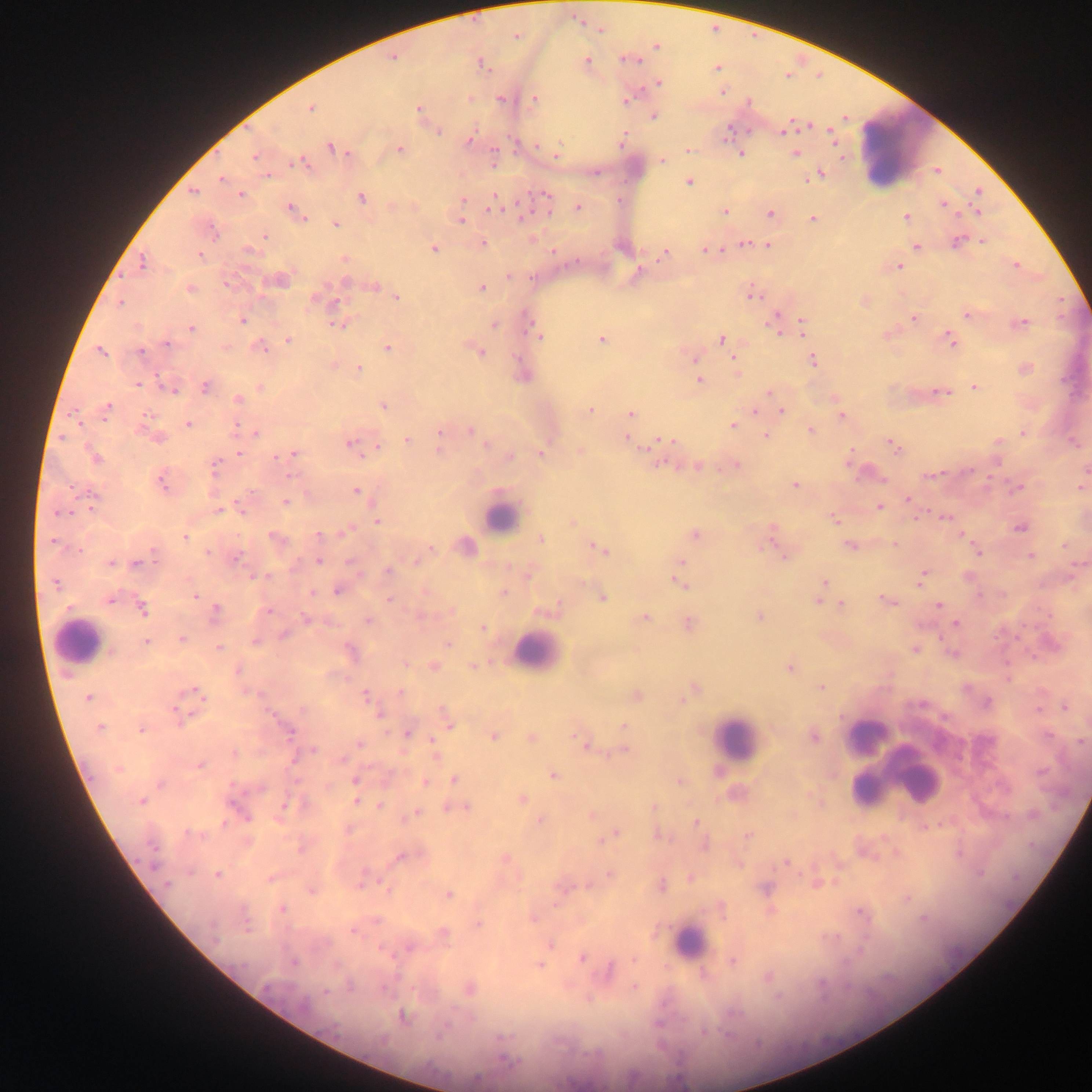
Approximate centers as (x, y) in pixels.
Summary:
  - Malaria parasite locations: (600, 30), (517, 36), (656, 47), (393, 58), (631, 60), (586, 61), (482, 65), (717, 67), (658, 83), (722, 91), (503, 100), (535, 100), (627, 101), (419, 108), (311, 109), (653, 116), (785, 129), (438, 130), (729, 130), (831, 132), (470, 138), (622, 141), (332, 148), (399, 149), (689, 149), (741, 154), (795, 154), (556, 155), (253, 157), (661, 160), (297, 163), (820, 174), (221, 179), (689, 182), (979, 190), (193, 192), (241, 195), (545, 195), (361, 198), (463, 199), (495, 204), (944, 204), (578, 206), (291, 208), (725, 211), (976, 211), (296, 212), (769, 213), (906, 217), (813, 218), (461, 221), (336, 224), (265, 237), (982, 241), (957, 242), (483, 244), (745, 244), (768, 245), (917, 246), (434, 248), (250, 251), (708, 251), (665, 254), (199, 255), (345, 259), (142, 263), (1015, 266), (899, 267), (280, 280), (346, 282), (227, 284), (374, 286), (482, 288), (191, 289), (753, 295), (396, 296), (316, 299), (120, 302), (967, 315), (775, 318), (913, 319), (242, 321), (1021, 322), (803, 324), (340, 325), (495, 325), (533, 326), (191, 328), (537, 334), (288, 340), (601, 340), (722, 340), (950, 340), (167, 343), (260, 346), (387, 347), (101, 351), (141, 353), (480, 353), (695, 359), (813, 360), (358, 369), (1025, 369), (700, 381), (139, 383), (205, 387), (975, 387), (169, 388), (260, 389), (941, 391), (770, 393), (238, 399), (383, 406), (108, 407), (590, 410), (755, 411), (782, 411), (631, 415), (841, 416), (189, 424), (732, 424), (236, 427), (470, 431), (811, 431), (440, 432), (256, 433), (1023, 433), (155, 436), (766, 436), (407, 439), (628, 439), (668, 440), (1075, 443), (349, 444), (487, 444), (894, 445), (378, 447), (440, 450), (580, 451), (541, 452), (239, 453), (293, 454), (285, 456), (96, 457), (510, 457), (736, 465), (214, 466), (698, 467), (1086, 469), (970, 471), (931, 476), (161, 483), (795, 485), (1017, 488), (1081, 488), (356, 491), (93, 497), (908, 499), (285, 502), (879, 507), (217, 510), (243, 511), (61, 513), (945, 517), (834, 520), (377, 521), (572, 522), (1020, 527), (345, 532), (318, 534), (694, 534), (185, 537), (275, 537), (540, 539), (771, 540), (53, 542), (466, 545), (850, 546), (430, 547), (776, 548), (601, 549), (208, 553), (979, 553), (783, 555), (1030, 555), (238, 557), (319, 561), (417, 561), (111, 563), (681, 563), (136, 564), (388, 572), (265, 575), (258, 577), (921, 579), (823, 582), (680, 583), (56, 584), (338, 591), (503, 592), (312, 593), (194, 595), (602, 597), (111, 600), (388, 600), (887, 601), (818, 602), (842, 605), (938, 606), (143, 609), (267, 611), (215, 612), (760, 616), (644, 618), (306, 619), (368, 621), (688, 623), (956, 623), (482, 627), (284, 635), (182, 639), (146, 642), (255, 642), (447, 643), (219, 648), (915, 650), (351, 653), (953, 653), (434, 666), (473, 666), (789, 669), (238, 671), (821, 688), (694, 689), (196, 691), (400, 692), (365, 695), (637, 696), (88, 697), (683, 700), (987, 702), (923, 704), (1064, 707), (303, 709), (1039, 709), (443, 711), (177, 712), (379, 716), (449, 725), (623, 725), (100, 727), (141, 729), (289, 731), (407, 734), (1048, 735), (493, 737), (814, 737), (531, 738), (1082, 742), (583, 743), (360, 744), (314, 751), (625, 751), (235, 753), (435, 755), (200, 765), (117, 770), (552, 776), (455, 779), (355, 780), (679, 781), (425, 782), (160, 783), (261, 788), (521, 799), (357, 800), (141, 801), (285, 805), (380, 806), (654, 806), (466, 807), (415, 814), (592, 814), (540, 820), (696, 823), (189, 833), (615, 835), (749, 836), (300, 850), (401, 857), (786, 862), (154, 865), (218, 874), (610, 874), (166, 884), (661, 886), (766, 888), (387, 889), (312, 890), (448, 894), (282, 908), (860, 912), (376, 921), (478, 923), (354, 931), (444, 933), (550, 943), (410, 948), (581, 958), (293, 962), (732, 962), (539, 965), (610, 970), (634, 987), (469, 989), (326, 991), (303, 1005), (402, 1017), (704, 1031), (440, 1035), (505, 1060)
  - Leukocyte locations: (904, 150), (500, 516), (77, 640), (535, 652), (866, 736), (736, 740), (902, 771), (865, 789), (688, 941)
  - Country: Ghana
  - Field of view: single
  - Capture: mobile-phone photograph through a microscope
  - Preparation: thick blood film
  - Image size: 1092×1092 pixels